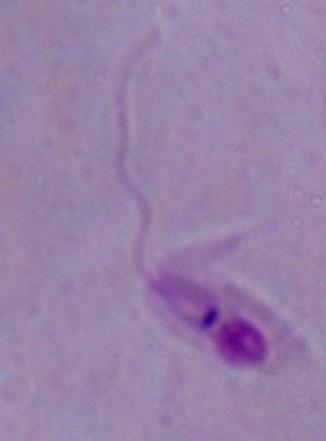

magnification: 1000x
identification: Leishmania
modality: micrograph